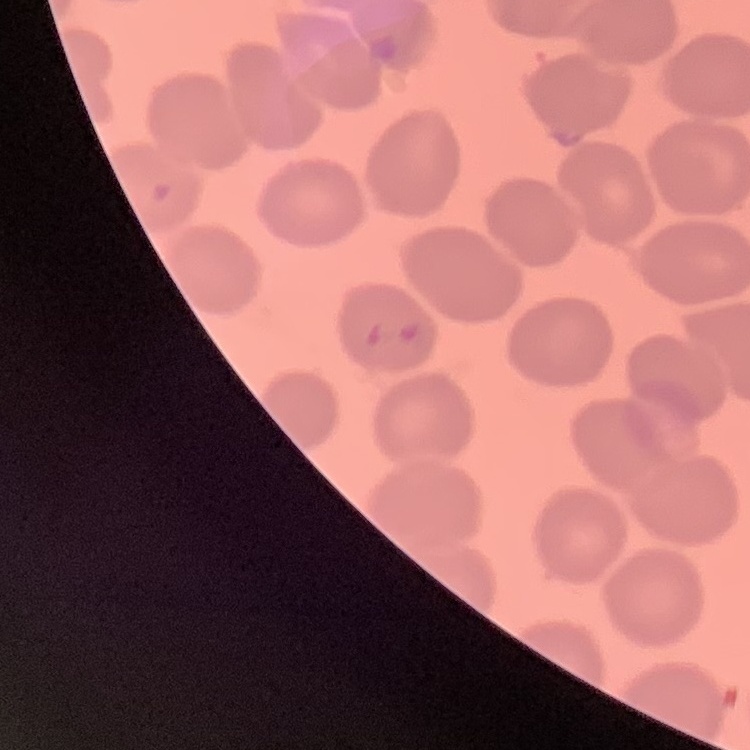
The erythrocytes exhibit no rouleaux formation. Stained with either Field's or Giemsa. One tile cut from a larger photomicrograph. Thin blood smear.